Assess the morphology of the erythrocytes.
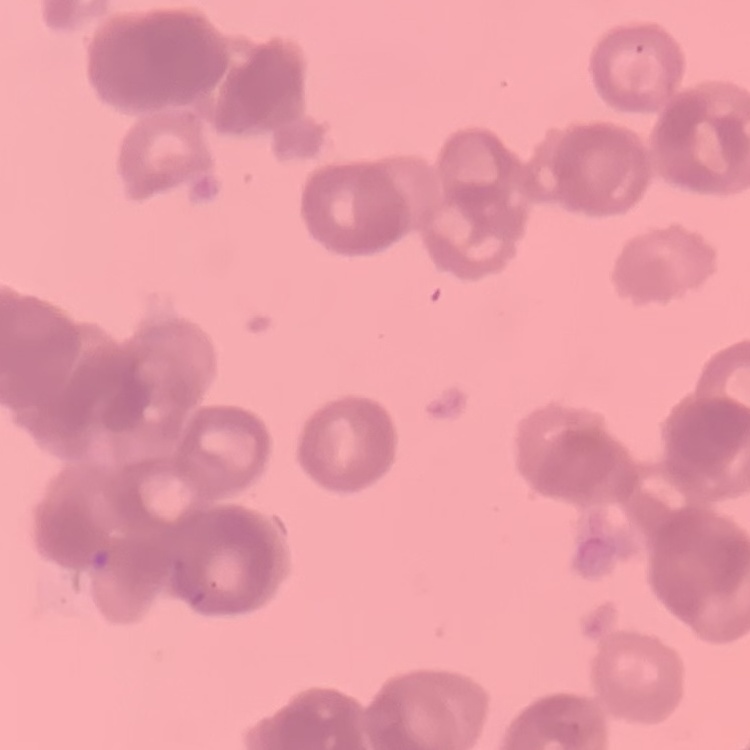

They show rouleaux formation.

One tile cut from a larger photomicrograph. Thin peripheral smear. Field's or Giemsa stain.